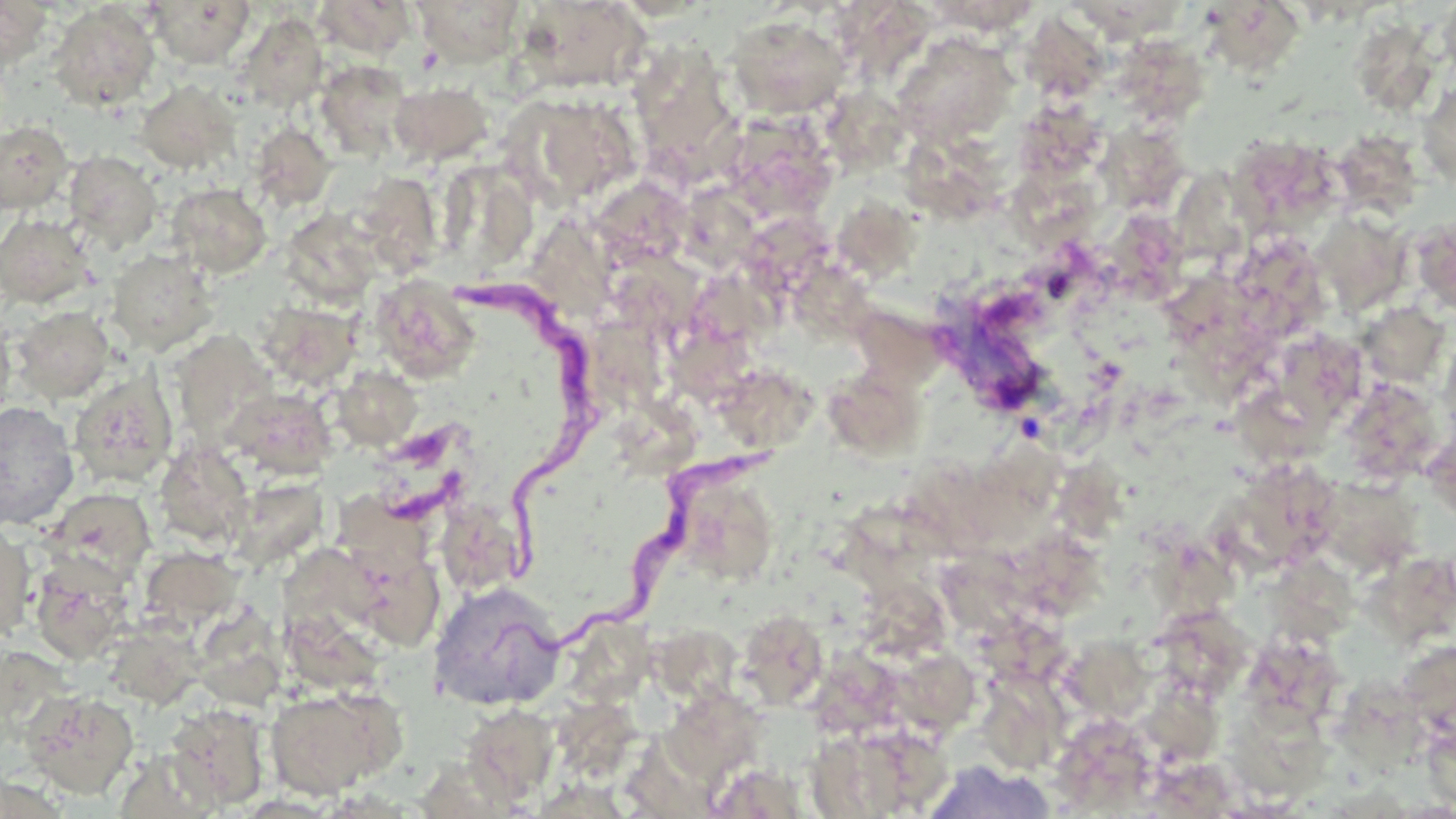

slide-level diagnosis = Trypanosoma brucei
stain = May-Grünwald-Giemsa
Trypanosoma brucei locations = approximate bounding boxes as (x1,y1)-(x2,y2) corner pairs in pixels: (456,269)-(589,589), (492,419)-(799,671), (343,495)-(441,591)
field of view = one of a larger specimen
preparation = thin blood smear
modality = optical microscopy
magnification = 1000x
image size = 1456×819 pixels
uninfected red blood cell locations = approximate bounding boxes as (x1,y1)-(x2,y2) corner pairs in pixels: (0,0)-(55,71), (313,0)-(416,60), (412,0)-(527,66), (516,0)-(651,94), (1437,0)-(1456,87), (147,1)-(255,67), (48,2)-(162,111), (838,2)-(942,74), (1082,3)-(1192,50), (1212,5)-(1318,92), (235,12)-(329,112), (725,14)-(851,120), (1020,15)-(1106,96), (1361,27)-(1443,120), (892,33)-(1018,149), (628,45)-(746,187), (1126,53)-(1212,125), (315,60)-(415,158), (135,80)-(239,175), (1417,80)-(1456,190), (389,81)-(494,165), (511,94)-(642,207), (830,97)-(916,178), (1018,103)-(1111,175), (718,110)-(840,225), (0,119)-(74,214), (249,122)-(337,211), (1223,125)-(1338,242), (1095,132)-(1188,214), (1339,136)-(1424,222), (904,143)-(1018,231), (63,151)-(163,254), (449,167)-(542,263), (1186,167)-(1267,279), (367,173)-(445,279), (1012,173)-(1111,254), (597,179)-(700,266), (167,183)-(272,278), (838,190)-(926,283), (690,195)-(771,269), (1117,210)-(1189,306), (281,212)-(373,301), (0,213)-(94,307), (737,214)-(847,298), (1410,215)-(1456,317), (544,224)-(634,320), (1322,227)-(1414,318), (1243,247)-(1331,342), (107,249)-(218,356), (792,263)-(885,349), (618,267)-(723,334), (369,275)-(481,383), (709,286)-(798,356), (256,301)-(361,389), (858,303)-(964,387), (11,306)-(115,403), (1362,310)-(1455,392), (0,311)-(16,427), (580,320)-(670,412), (1193,328)-(1282,407), (1296,345)-(1371,430), (676,346)-(770,411), (333,366)-(422,451), (69,371)-(178,488), (728,384)-(819,456), (1354,384)-(1448,487), (837,387)-(936,462), (224,388)-(335,480), (1241,393)-(1341,481), (0,401)-(79,531), (611,412)-(704,482), (153,441)-(254,546), (240,467)-(340,566), (1255,474)-(1335,572), (1074,475)-(1145,541), (1338,484)-(1422,584), (42,486)-(156,586), (690,501)-(779,600), (446,510)-(509,592), (833,514)-(957,607), (0,519)-(37,644), (1359,534)-(1456,643), (1145,545)-(1249,633), (138,546)-(244,634), (1018,546)-(1119,635), (29,553)-(137,665), (946,558)-(1032,639), (1264,566)-(1365,654), (427,580)-(566,711), (870,593)-(950,666), (288,609)-(387,688), (735,609)-(830,711), (572,612)-(665,703), (963,616)-(1081,698), (649,619)-(757,702), (106,620)-(204,708), (1169,624)-(1251,711), (224,625)-(296,703), (1059,628)-(1158,742), (1390,636)-(1456,730), (1258,649)-(1341,726), (815,651)-(898,741), (902,664)-(980,733), (1331,676)-(1432,786), (992,678)-(1067,777), (1145,683)-(1223,770), (1223,684)-(1334,806), (264,685)-(402,798), (21,690)-(140,799), (662,691)-(761,785), (165,703)-(271,810), (461,703)-(559,805), (558,703)-(641,774), (1423,721)-(1456,814), (806,723)-(948,818), (1056,727)-(1156,814), (614,733)-(719,816), (918,760)-(1060,819)